Outline each blood parasite and name the species.
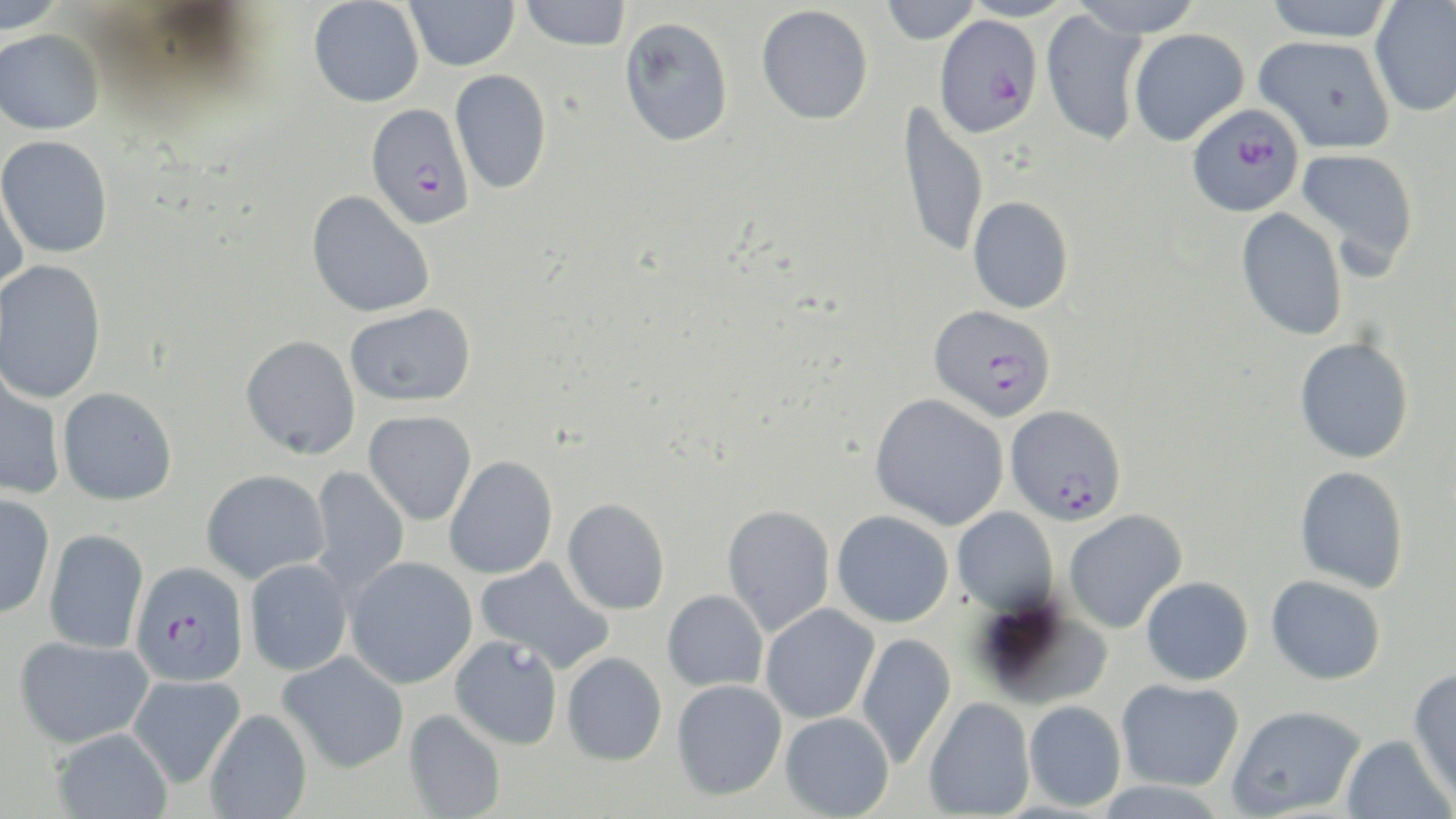

Approximate bounding boxes as named x1/y1/x2/y2 corners in pixels.
Plasmodium falciparum-infected red blood cells: (x1=934, y1=14, x2=1043, y2=138), (x1=1186, y1=102, x2=1305, y2=218), (x1=365, y1=103, x2=474, y2=229), (x1=928, y1=305, x2=1056, y2=421), (x1=1005, y1=404, x2=1127, y2=525), (x1=129, y1=560, x2=250, y2=687).
No Plasmodium ovale, Plasmodium malariae, Plasmodium vivax, Babesia divergens, or Trypanosoma brucei observed.

Summary:
  - Uninfected red blood cell locations: (x1=0, y1=0, x2=67, y2=33), (x1=404, y1=0, x2=520, y2=71), (x1=519, y1=0, x2=631, y2=51), (x1=879, y1=0, x2=982, y2=45), (x1=957, y1=0, x2=1077, y2=22), (x1=1070, y1=0, x2=1205, y2=38), (x1=1261, y1=0, x2=1398, y2=42), (x1=308, y1=1, x2=424, y2=108), (x1=1369, y1=1, x2=1456, y2=117), (x1=756, y1=4, x2=873, y2=125), (x1=1039, y1=8, x2=1150, y2=147), (x1=619, y1=16, x2=734, y2=146), (x1=1128, y1=28, x2=1249, y2=146), (x1=0, y1=29, x2=104, y2=134), (x1=1253, y1=35, x2=1396, y2=154), (x1=450, y1=69, x2=552, y2=195), (x1=897, y1=100, x2=990, y2=260), (x1=0, y1=135, x2=114, y2=258), (x1=1294, y1=147, x2=1418, y2=273), (x1=0, y1=171, x2=28, y2=299), (x1=306, y1=190, x2=434, y2=318), (x1=967, y1=196, x2=1073, y2=314), (x1=1236, y1=207, x2=1348, y2=341), (x1=0, y1=259, x2=107, y2=404), (x1=345, y1=303, x2=475, y2=406), (x1=240, y1=334, x2=360, y2=459), (x1=1294, y1=337, x2=1414, y2=464), (x1=0, y1=369, x2=66, y2=500), (x1=57, y1=386, x2=177, y2=505), (x1=869, y1=393, x2=1009, y2=530), (x1=364, y1=410, x2=477, y2=525), (x1=444, y1=456, x2=558, y2=579), (x1=1294, y1=465, x2=1409, y2=593), (x1=310, y1=466, x2=409, y2=599), (x1=201, y1=469, x2=329, y2=584), (x1=0, y1=494, x2=55, y2=620), (x1=561, y1=499, x2=670, y2=615), (x1=721, y1=504, x2=835, y2=637), (x1=952, y1=507, x2=1059, y2=615), (x1=1063, y1=509, x2=1187, y2=634), (x1=832, y1=510, x2=953, y2=627), (x1=43, y1=529, x2=149, y2=654), (x1=475, y1=556, x2=614, y2=673), (x1=345, y1=557, x2=477, y2=689), (x1=244, y1=559, x2=352, y2=676), (x1=1266, y1=575, x2=1386, y2=685), (x1=1141, y1=576, x2=1254, y2=686), (x1=662, y1=590, x2=768, y2=692), (x1=974, y1=597, x2=1116, y2=711), (x1=760, y1=604, x2=879, y2=724), (x1=856, y1=632, x2=956, y2=770), (x1=450, y1=635, x2=563, y2=750), (x1=13, y1=636, x2=153, y2=748), (x1=278, y1=651, x2=410, y2=773), (x1=562, y1=652, x2=667, y2=766), (x1=1408, y1=668, x2=1456, y2=803), (x1=127, y1=674, x2=245, y2=789), (x1=1116, y1=678, x2=1244, y2=791), (x1=671, y1=680, x2=787, y2=801), (x1=923, y1=697, x2=1036, y2=818), (x1=1023, y1=700, x2=1126, y2=811), (x1=1227, y1=704, x2=1366, y2=817), (x1=204, y1=708, x2=312, y2=819), (x1=403, y1=709, x2=506, y2=819), (x1=780, y1=712, x2=895, y2=818), (x1=51, y1=728, x2=173, y2=819), (x1=1341, y1=734, x2=1454, y2=819), (x1=1091, y1=780, x2=1228, y2=819)
  - Slide-level diagnosis: Plasmodium falciparum
  - Stain: May-Grünwald-Giemsa
  - Magnification: 1000x
  - Image size: 1456×819 pixels
  - Preparation: thin blood smear
  - Modality: optical microscopy
  - Field of view: one of a larger specimen